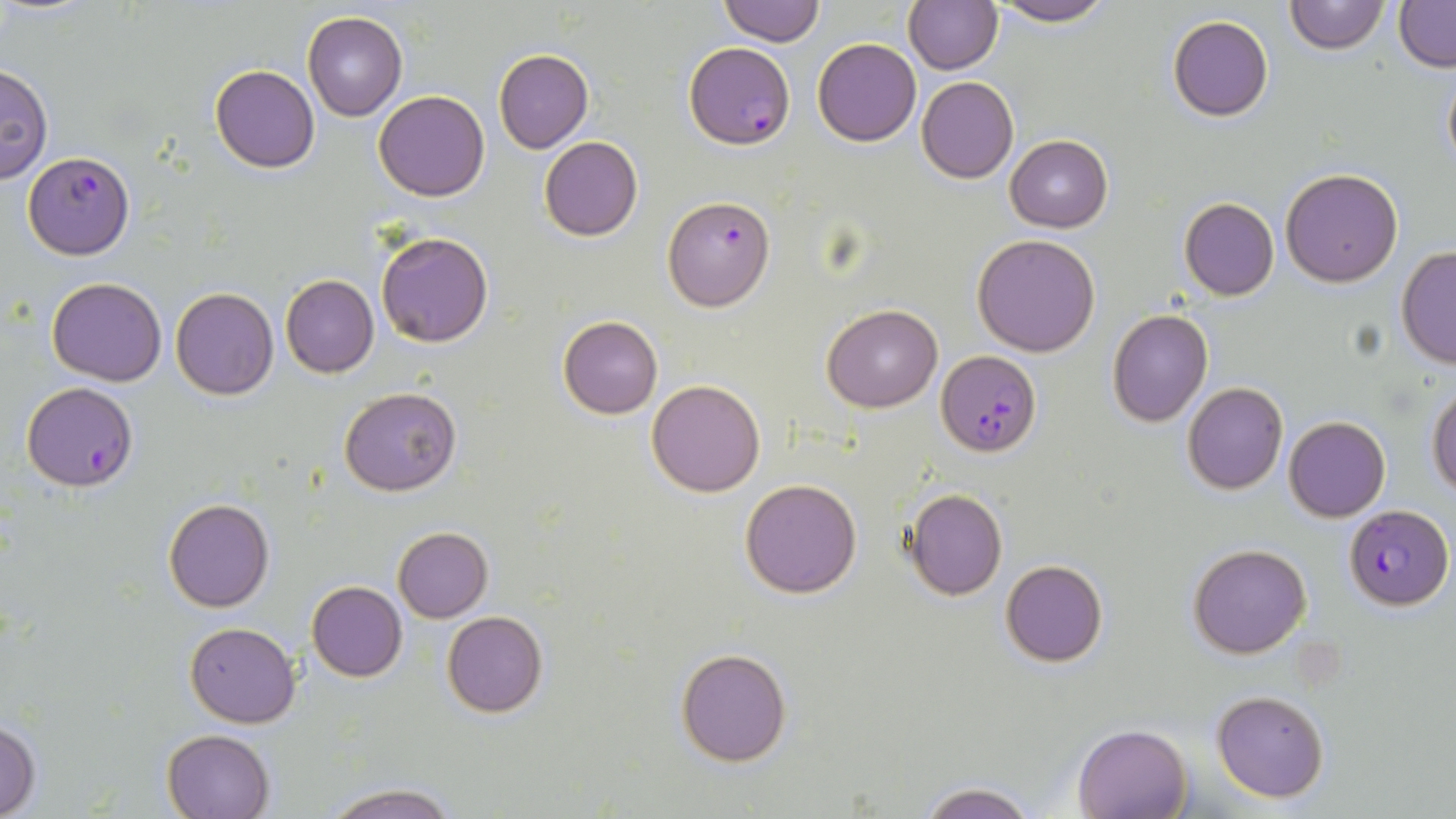

slide-level diagnosis = Plasmodium falciparum
stain = May-Grünwald-Giemsa
field of view = single
modality = optical microscopy
preparation = thin blood smear
Plasmodium falciparum-infected red blood cell locations = approximate bounding boxes as [x1, y1, x2, y2] in pixels: [685, 43, 792, 149], [24, 150, 132, 260], [662, 196, 775, 312], [936, 349, 1042, 457], [21, 382, 137, 491], [1345, 503, 1453, 611]
magnification = 1000x
uninfected red blood cell locations = approximate bounding boxes as [x1, y1, x2, y2] in pixels: [716, 0, 827, 48], [903, 0, 1003, 74], [1283, 0, 1388, 55], [1393, 0, 1456, 70], [988, 1, 1115, 26], [302, 12, 408, 122], [1168, 15, 1274, 122], [812, 37, 922, 147], [493, 49, 593, 153], [210, 64, 320, 173], [1441, 64, 1456, 176], [0, 65, 52, 184], [916, 76, 1019, 184], [375, 90, 489, 202], [538, 136, 643, 241], [1007, 136, 1112, 232], [1280, 168, 1403, 288], [1178, 197, 1279, 301], [376, 230, 494, 348], [972, 234, 1101, 356], [1396, 247, 1456, 366], [281, 275, 379, 377], [45, 278, 167, 386], [170, 286, 278, 400], [823, 305, 942, 412], [1107, 309, 1212, 428], [557, 315, 663, 419], [646, 380, 765, 497], [1183, 383, 1288, 495], [1428, 386, 1456, 495], [339, 388, 459, 495], [1284, 416, 1390, 522], [740, 479, 862, 598], [904, 488, 1008, 600], [163, 499, 275, 613], [393, 526, 493, 621], [1187, 543, 1311, 659], [1001, 560, 1108, 667], [307, 581, 408, 681], [442, 610, 548, 717], [185, 622, 299, 729], [674, 647, 792, 767], [1211, 689, 1330, 803], [0, 718, 41, 818], [1072, 723, 1193, 819], [162, 731, 274, 816], [318, 781, 461, 819], [912, 781, 1041, 819]
image size = 1456×819 pixels